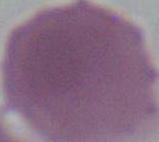
Micrograph. An erythrocyte is shown. Captured at 1000x magnification.